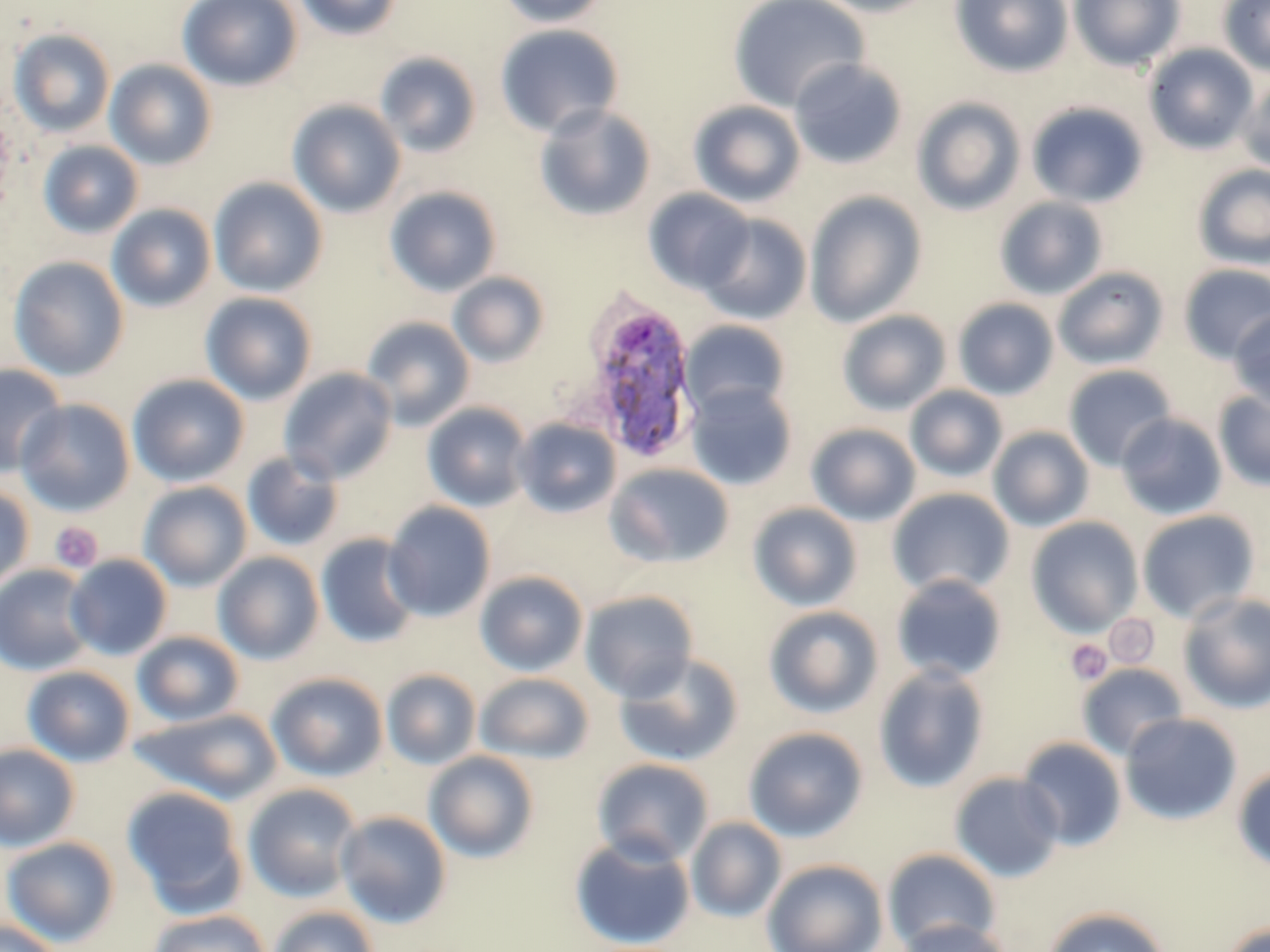

Plasmodium ovale-infected red blood cell locations = approximate bounding boxes as named x1/y1/x2/y2 corners in pixels: (x1=580, y1=296, x2=701, y2=464)
slide-level diagnosis = Plasmodium ovale
modality = light microscopy
magnification = 1000x
uninfected red blood cell locations (subset) = approximate bounding boxes as named x1/y1/x2/y2 corners in pixels: (x1=178, y1=0, x2=302, y2=91), (x1=293, y1=0, x2=403, y2=40), (x1=497, y1=0, x2=610, y2=28), (x1=728, y1=0, x2=871, y2=112), (x1=809, y1=0, x2=941, y2=17), (x1=950, y1=0, x2=1073, y2=78), (x1=1068, y1=0, x2=1186, y2=71), (x1=1218, y1=0, x2=1270, y2=77), (x1=494, y1=24, x2=624, y2=138), (x1=8, y1=28, x2=116, y2=137), (x1=1143, y1=43, x2=1259, y2=154), (x1=374, y1=51, x2=482, y2=158), (x1=789, y1=57, x2=908, y2=170), (x1=104, y1=59, x2=217, y2=170), (x1=1238, y1=77, x2=1270, y2=175), (x1=911, y1=97, x2=1026, y2=216), (x1=287, y1=99, x2=407, y2=218), (x1=688, y1=100, x2=807, y2=207), (x1=1026, y1=101, x2=1150, y2=208), (x1=533, y1=104, x2=657, y2=222), (x1=38, y1=140, x2=143, y2=239), (x1=1192, y1=164, x2=1270, y2=268), (x1=209, y1=177, x2=328, y2=296), (x1=384, y1=185, x2=502, y2=297), (x1=643, y1=188, x2=755, y2=294), (x1=804, y1=191, x2=927, y2=328), (x1=994, y1=196, x2=1109, y2=300), (x1=106, y1=204, x2=216, y2=313), (x1=699, y1=212, x2=812, y2=324), (x1=7, y1=256, x2=129, y2=382), (x1=1179, y1=264, x2=1270, y2=362), (x1=1052, y1=267, x2=1169, y2=369), (x1=448, y1=272, x2=550, y2=368), (x1=200, y1=292, x2=317, y2=405), (x1=952, y1=298, x2=1059, y2=400), (x1=1228, y1=309, x2=1270, y2=410), (x1=837, y1=310, x2=951, y2=416), (x1=360, y1=316, x2=476, y2=430), (x1=680, y1=320, x2=791, y2=419), (x1=0, y1=363, x2=67, y2=478), (x1=1063, y1=364, x2=1177, y2=471), (x1=278, y1=367, x2=398, y2=484), (x1=126, y1=374, x2=249, y2=487), (x1=685, y1=382, x2=799, y2=490), (x1=905, y1=385, x2=1008, y2=483), (x1=1213, y1=390, x2=1270, y2=492), (x1=16, y1=398, x2=136, y2=516), (x1=422, y1=402, x2=531, y2=512), (x1=1116, y1=413, x2=1227, y2=520), (x1=512, y1=418, x2=622, y2=518), (x1=806, y1=423, x2=921, y2=526), (x1=988, y1=426, x2=1095, y2=531), (x1=241, y1=451, x2=345, y2=553), (x1=606, y1=462, x2=735, y2=569), (x1=139, y1=481, x2=252, y2=591), (x1=0, y1=484, x2=34, y2=590), (x1=888, y1=487, x2=1015, y2=597), (x1=383, y1=502, x2=496, y2=622), (x1=747, y1=502, x2=863, y2=611), (x1=1136, y1=509, x2=1260, y2=623), (x1=1026, y1=517, x2=1144, y2=637), (x1=315, y1=533, x2=421, y2=649), (x1=213, y1=551, x2=324, y2=664), (x1=64, y1=554, x2=172, y2=660), (x1=1, y1=564, x2=96, y2=676), (x1=475, y1=570, x2=588, y2=676), (x1=891, y1=574, x2=1007, y2=683), (x1=580, y1=590, x2=699, y2=703), (x1=1177, y1=592, x2=1270, y2=714), (x1=763, y1=605, x2=884, y2=719), (x1=132, y1=631, x2=244, y2=727), (x1=613, y1=653, x2=744, y2=767), (x1=872, y1=663, x2=990, y2=793), (x1=1077, y1=663, x2=1188, y2=760), (x1=22, y1=665, x2=135, y2=767), (x1=381, y1=669, x2=481, y2=770), (x1=268, y1=672, x2=388, y2=781), (x1=475, y1=672, x2=595, y2=764), (x1=130, y1=708, x2=283, y2=805), (x1=1120, y1=712, x2=1243, y2=825), (x1=743, y1=726, x2=869, y2=842), (x1=1017, y1=737, x2=1127, y2=850), (x1=0, y1=743, x2=80, y2=851), (x1=423, y1=750, x2=540, y2=863), (x1=591, y1=758, x2=714, y2=866), (x1=1231, y1=764, x2=1270, y2=872), (x1=949, y1=772, x2=1065, y2=882), (x1=243, y1=783, x2=362, y2=901), (x1=121, y1=785, x2=248, y2=916), (x1=335, y1=810, x2=452, y2=929), (x1=686, y1=817, x2=787, y2=921), (x1=569, y1=835, x2=696, y2=950), (x1=1, y1=836, x2=120, y2=946), (x1=882, y1=848, x2=1001, y2=951), (x1=762, y1=859, x2=888, y2=952), (x1=267, y1=905, x2=379, y2=952), (x1=1042, y1=906, x2=1171, y2=952), (x1=147, y1=909, x2=272, y2=952), (x1=896, y1=918, x2=1012, y2=952), (x1=1217, y1=919, x2=1270, y2=952), (x1=0, y1=920, x2=69, y2=952)
platelet locations (subset) = approximate bounding boxes as named x1/y1/x2/y2 corners in pixels: (x1=49, y1=522, x2=103, y2=573), (x1=1065, y1=639, x2=1112, y2=685)
preparation = thin blood film
image size = 1270×952 pixels
field of view = single
stain = May-Grünwald-Giemsa